Report the malaria status of this cell.
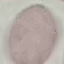
It is uninfected.

capture = smartphone through the microscope eyepiece
image type = cell patch, automatically extracted from a larger field of view and resized to 64 × 64 pixels
preparation = thin smear
stain = Giemsa